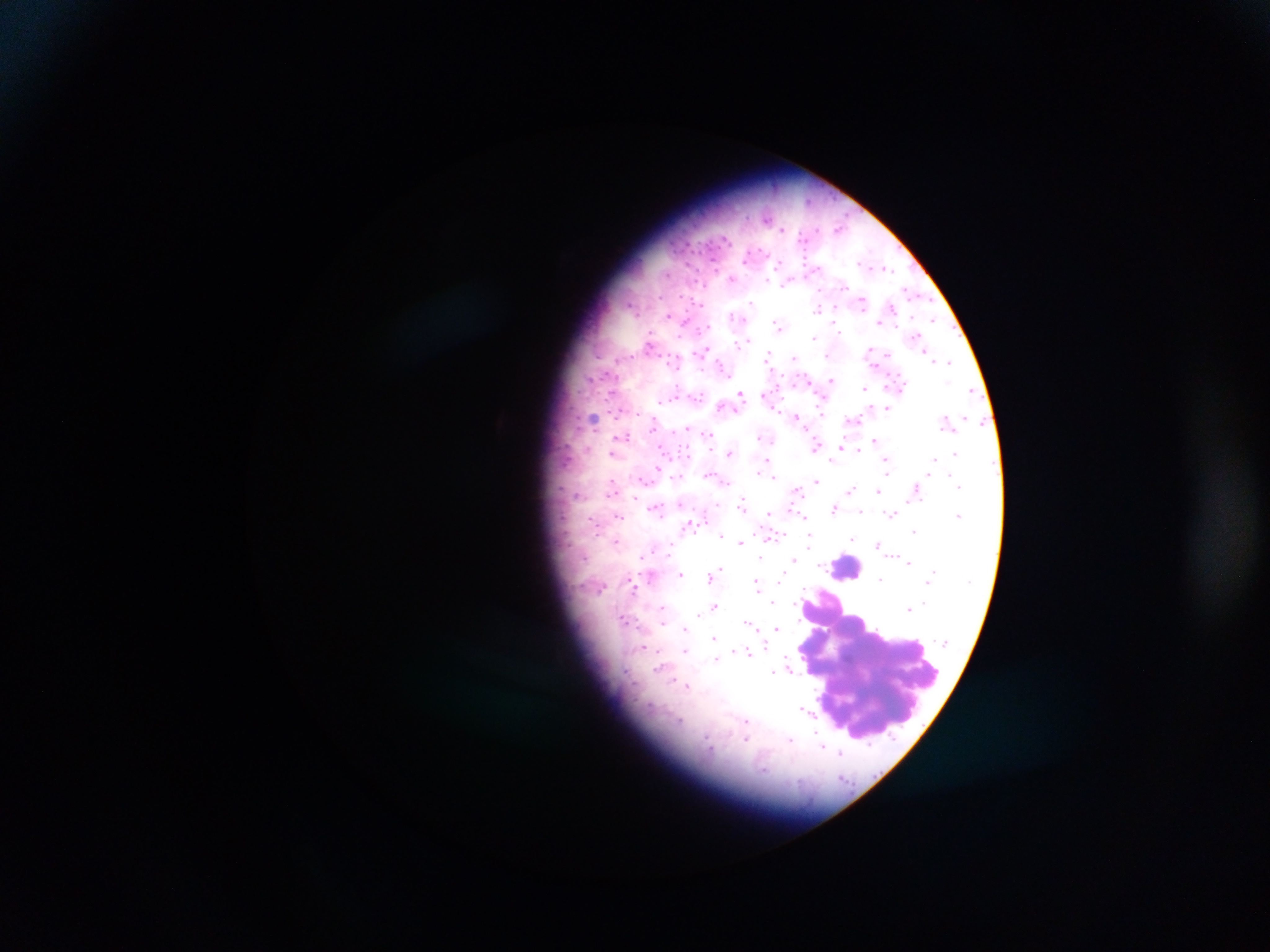
image_size: 1270×952 pixels
plasmodium_parasite_locations: 'approximate centers as [x, y] in pixels: [767, 219], [840, 228], [724, 239], [778, 264], [886, 268], [667, 273], [732, 279], [767, 280], [785, 284], [844, 287], [907, 291], [926, 300], [862, 302], [751, 303], [700, 304], [630, 305], [890, 306], [818, 309], [669, 315], [734, 317], [934, 320], [879, 322], [777, 325], [838, 329], [815, 337], [918, 338], [747, 340], [649, 342], [738, 345], [704, 350], [870, 351], [768, 354], [826, 355], [887, 355], [795, 358], [949, 361], [723, 367], [589, 376], [831, 380], [865, 388], [971, 391], [612, 393], [740, 394], [697, 395], [661, 401], [724, 405], [737, 408], [887, 409], [621, 411], [797, 417], [593, 419], [853, 420], [654, 423], [687, 427], [678, 431], [708, 434], [625, 436], [761, 437], [874, 440], [816, 446], [842, 448], [859, 448], [587, 449], [662, 451], [729, 452], [612, 454], [955, 454], [886, 458], [934, 458], [832, 459], [766, 460], [658, 467], [887, 470], [759, 472], [928, 474], [707, 475], [953, 475], [678, 476], [772, 476], [726, 481], [817, 481], [612, 483], [958, 486], [852, 488], [913, 488], [611, 490], [797, 491], [878, 491], [578, 495], [635, 496], [637, 500], [742, 502], [716, 503], [681, 504], [655, 508], [834, 509], [860, 511], [768, 514], [890, 514], [959, 515], [619, 516], [591, 519], [804, 519], [807, 520], [914, 531], [598, 534], [720, 535], [774, 536], [810, 537], [853, 537], [616, 541], [740, 542], [809, 544], [878, 544], [668, 549], [584, 557], [640, 557], [760, 558], [793, 559], [909, 562], [720, 568], [713, 574], [783, 574], [651, 575], [681, 575], [709, 576], [881, 579], [756, 582], [927, 583], [634, 589], [773, 601], [663, 607], [715, 607], [907, 608], [699, 614], [623, 618], [663, 622], [747, 623], [776, 627], [684, 630], [714, 637], [642, 647], [685, 650], [733, 650], [748, 653], [716, 659], [787, 662], [659, 666], [790, 670], [773, 672], [625, 673], [671, 678], [688, 685], [806, 710], [679, 720], [747, 720], [746, 737], [790, 739], [706, 741], [821, 745], [841, 753]'
preparation: thick blood smear
leukocyte_locations: 'approximate centers as [x, y] in pixels: [845, 567], [872, 659]'
capture: mobile-phone photograph through a microscope
country: Ghana
field_of_view: single